Classify this cell by malaria status.
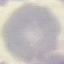

Uninfected.

Giemsa-stained preparation. Acquired by smartphone through the microscope eyepiece. Thin blood film. Cell patch, automatically extracted from a larger field of view and resized to 64 × 64 pixels.